State the preparation type.
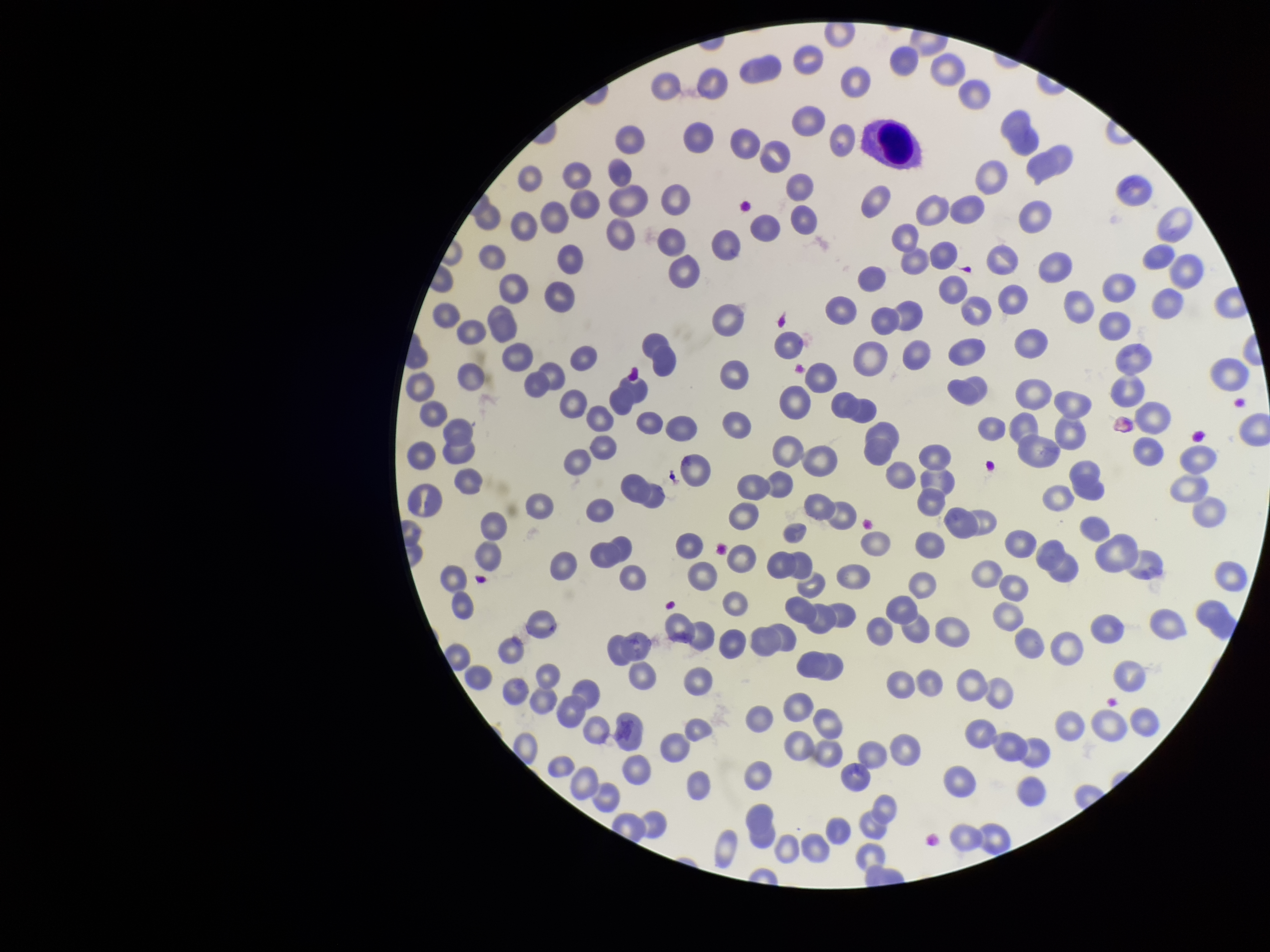

A thin smear.

species reported for this patient = Plasmodium vivax
stain = Giemsa
parasitized red blood cell count = 0
image size = 1270×952 pixels
capture = smartphone photograph through the microscope eyepiece
patient malaria status = infected
field of view = one from this slide
red blood cell count = 216
parasitized red blood cells = none seen